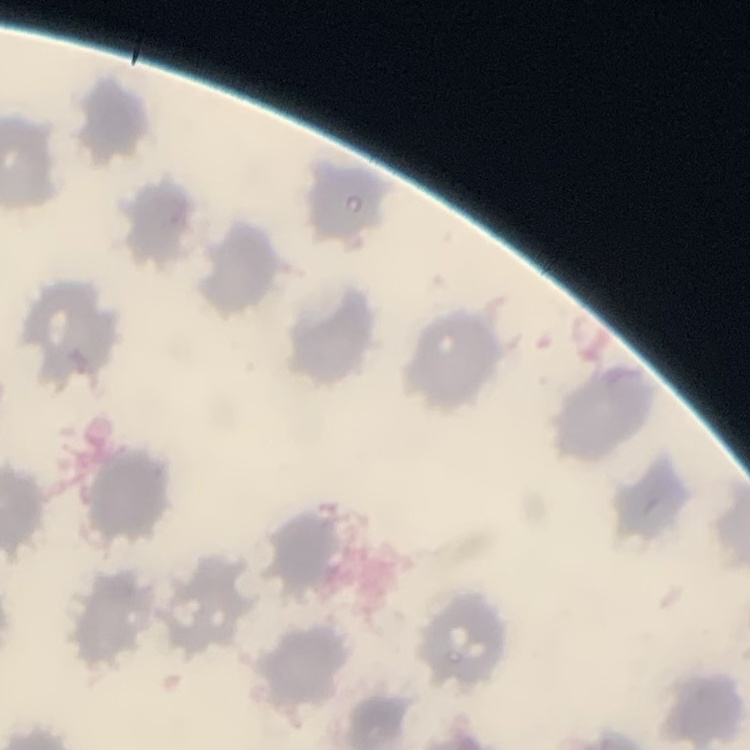

The erythrocytes show no rouleaux formation. Thin peripheral smear. Field's or Giemsa stain. Square crop of a larger photomicrograph.